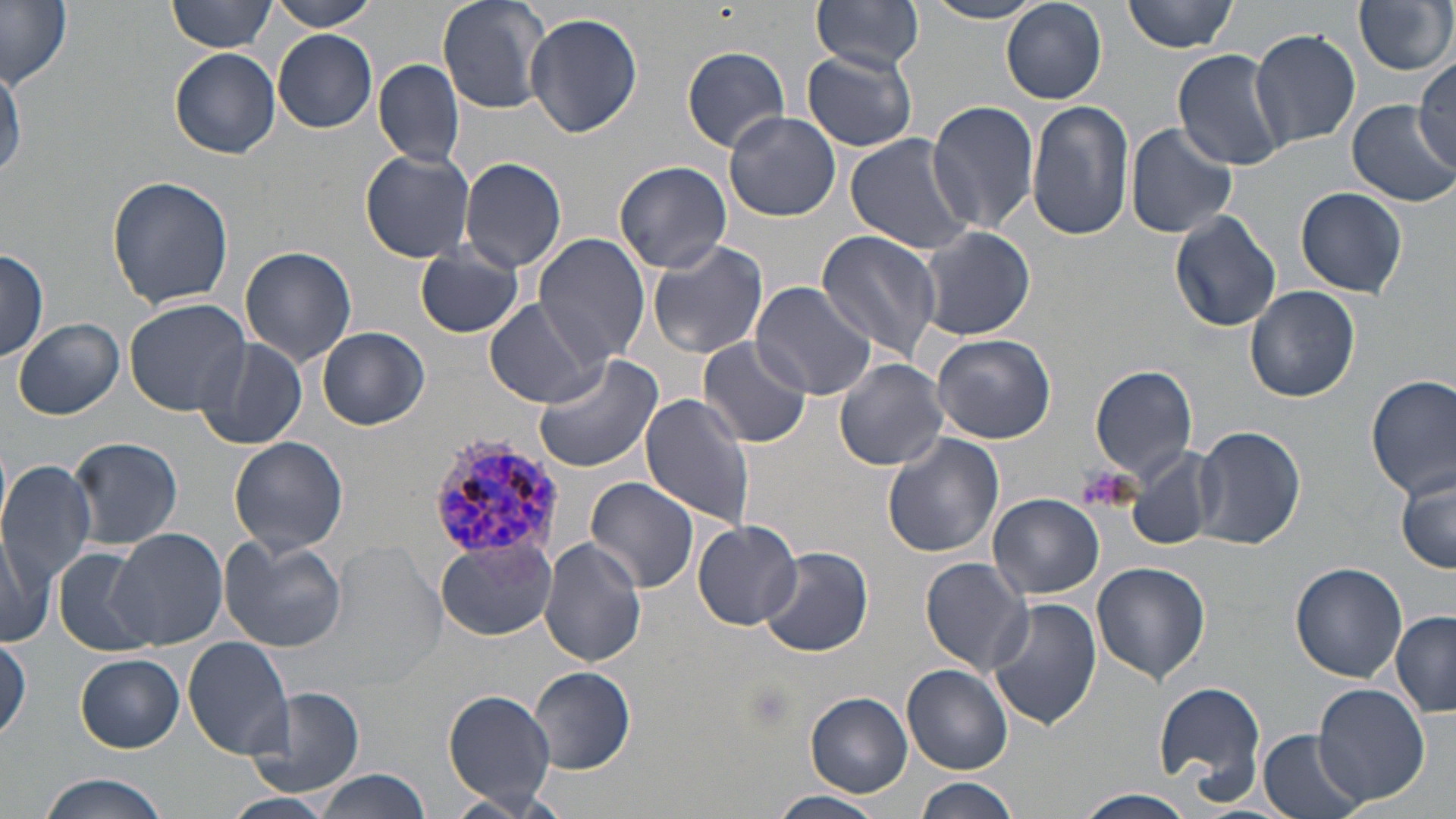

Summary:
  - Coordinate format: approximate bounding boxes as named x1/y1/x2/y2 corners in pixels
  - Platelet locations: (x1=1075, y1=461, x2=1134, y2=509)
  - Plasmodium vivax-infected red blood cell locations: (x1=428, y1=429, x2=567, y2=567)
  - Uninfected red blood cell locations: (x1=167, y1=0, x2=279, y2=54), (x1=267, y1=0, x2=379, y2=30), (x1=437, y1=0, x2=554, y2=115), (x1=811, y1=0, x2=926, y2=73), (x1=924, y1=0, x2=1046, y2=23), (x1=1000, y1=0, x2=1108, y2=105), (x1=1122, y1=0, x2=1239, y2=53), (x1=1354, y1=0, x2=1455, y2=77), (x1=0, y1=2, x2=73, y2=90), (x1=524, y1=13, x2=645, y2=139), (x1=1249, y1=29, x2=1361, y2=152), (x1=273, y1=31, x2=379, y2=132), (x1=681, y1=45, x2=792, y2=153), (x1=169, y1=48, x2=281, y2=159), (x1=1171, y1=49, x2=1287, y2=171), (x1=802, y1=50, x2=917, y2=152), (x1=0, y1=55, x2=23, y2=183), (x1=1414, y1=56, x2=1455, y2=166), (x1=373, y1=59, x2=465, y2=167), (x1=927, y1=99, x2=1042, y2=236), (x1=1028, y1=100, x2=1135, y2=241), (x1=1347, y1=101, x2=1455, y2=206), (x1=723, y1=110, x2=841, y2=221), (x1=1125, y1=123, x2=1238, y2=239), (x1=844, y1=133, x2=977, y2=255), (x1=360, y1=148, x2=476, y2=263), (x1=459, y1=157, x2=568, y2=274), (x1=614, y1=160, x2=732, y2=274), (x1=108, y1=174, x2=234, y2=310), (x1=1294, y1=186, x2=1407, y2=298), (x1=1169, y1=211, x2=1281, y2=331), (x1=919, y1=225, x2=1035, y2=341), (x1=815, y1=230, x2=941, y2=363), (x1=534, y1=233, x2=651, y2=364), (x1=646, y1=240, x2=769, y2=361), (x1=414, y1=244, x2=523, y2=338), (x1=240, y1=246, x2=357, y2=366), (x1=0, y1=247, x2=48, y2=358), (x1=749, y1=280, x2=878, y2=400), (x1=1245, y1=285, x2=1361, y2=402), (x1=124, y1=299, x2=253, y2=418), (x1=484, y1=299, x2=606, y2=407), (x1=14, y1=319, x2=124, y2=421), (x1=316, y1=327, x2=429, y2=431), (x1=932, y1=334, x2=1058, y2=444), (x1=190, y1=336, x2=307, y2=451), (x1=700, y1=337, x2=811, y2=451), (x1=533, y1=351, x2=663, y2=472), (x1=834, y1=357, x2=949, y2=470), (x1=1090, y1=364, x2=1198, y2=481), (x1=1367, y1=374, x2=1455, y2=500), (x1=641, y1=392, x2=761, y2=531), (x1=1193, y1=425, x2=1306, y2=550), (x1=881, y1=432, x2=1004, y2=558), (x1=68, y1=435, x2=185, y2=549), (x1=228, y1=436, x2=349, y2=556), (x1=1127, y1=448, x2=1219, y2=553), (x1=0, y1=459, x2=97, y2=588), (x1=1397, y1=471, x2=1456, y2=573), (x1=586, y1=476, x2=700, y2=593), (x1=988, y1=493, x2=1104, y2=600), (x1=693, y1=519, x2=801, y2=630), (x1=106, y1=529, x2=226, y2=649), (x1=0, y1=532, x2=53, y2=646), (x1=218, y1=535, x2=347, y2=651), (x1=539, y1=538, x2=648, y2=669), (x1=435, y1=540, x2=555, y2=642), (x1=757, y1=545, x2=872, y2=658), (x1=52, y1=546, x2=154, y2=656), (x1=326, y1=550, x2=443, y2=684), (x1=920, y1=557, x2=1033, y2=675), (x1=1091, y1=563, x2=1212, y2=684), (x1=1290, y1=563, x2=1409, y2=683), (x1=986, y1=598, x2=1102, y2=731), (x1=1391, y1=611, x2=1456, y2=714), (x1=0, y1=636, x2=30, y2=742), (x1=183, y1=637, x2=295, y2=758), (x1=77, y1=654, x2=185, y2=752), (x1=903, y1=665, x2=1012, y2=776), (x1=528, y1=666, x2=637, y2=774), (x1=807, y1=679, x2=1016, y2=785), (x1=1153, y1=682, x2=1266, y2=800), (x1=1314, y1=683, x2=1429, y2=807), (x1=247, y1=687, x2=366, y2=797), (x1=444, y1=691, x2=558, y2=807), (x1=807, y1=693, x2=913, y2=795), (x1=1258, y1=730, x2=1368, y2=819), (x1=316, y1=772, x2=432, y2=819), (x1=38, y1=774, x2=170, y2=819), (x1=912, y1=777, x2=1021, y2=819), (x1=1070, y1=789, x2=1196, y2=819), (x1=437, y1=790, x2=558, y2=819), (x1=770, y1=790, x2=887, y2=819), (x1=221, y1=793, x2=341, y2=819)
  - Slide-level diagnosis: Plasmodium vivax
  - Image size: 1456×819 pixels
  - Modality: optical microscopy
  - Preparation: thin blood film
  - Field of view: single
  - Magnification: 1000x
  - Stain: May-Grünwald-Giemsa